Comment on the morphology of the erythrocytes.
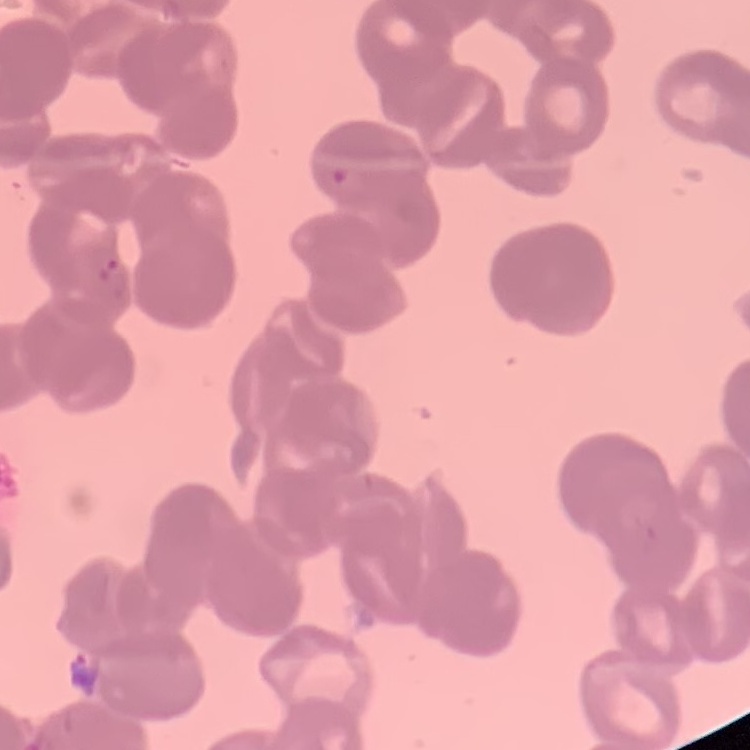
Rouleaux formation.

{
  "preparation": "thin peripheral smear",
  "image_type": "one tile cut from a larger photomicrograph",
  "stain": "Field's or Giemsa"
}